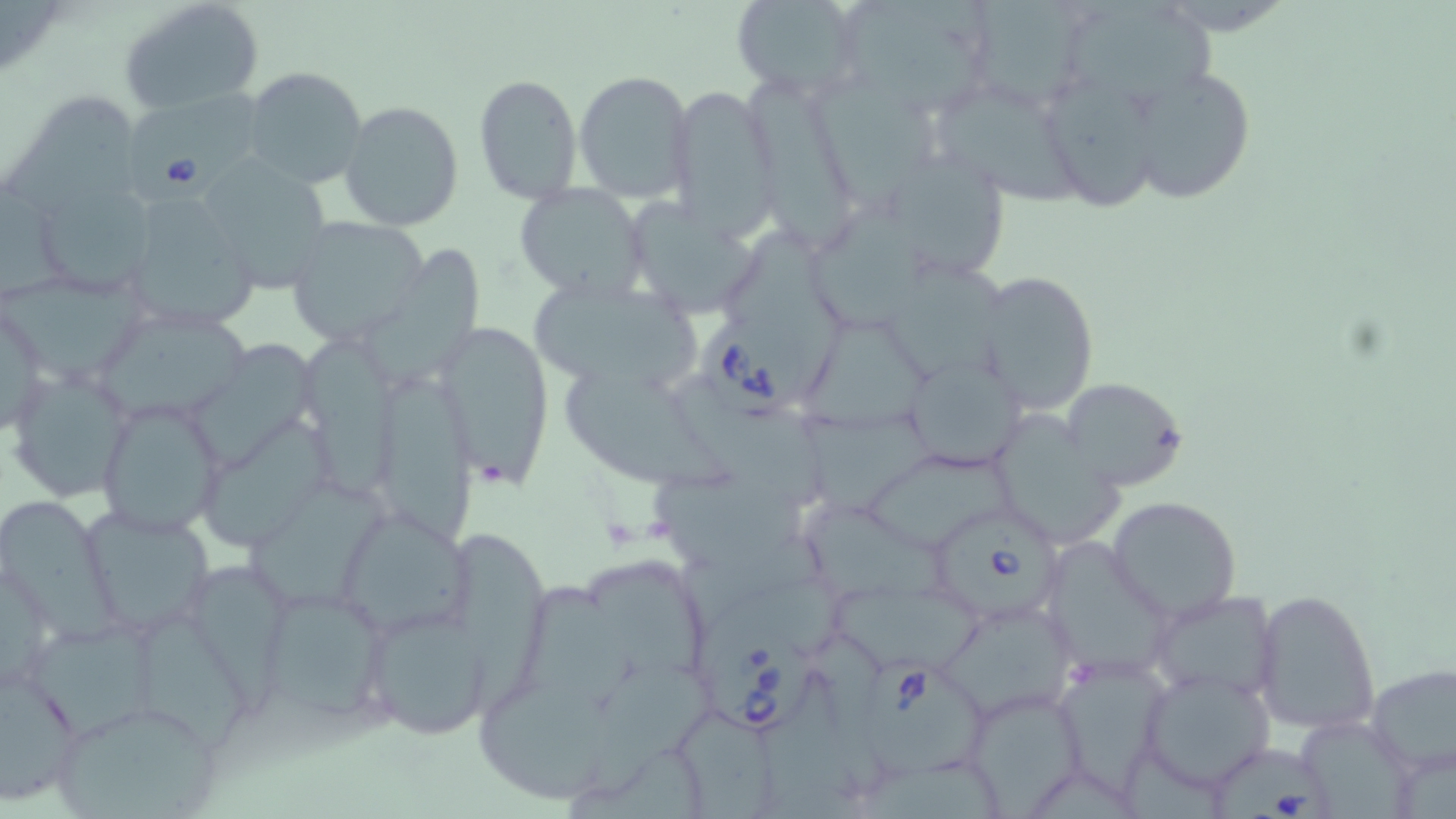

Approximate bounding boxes as [x1, y1, x2, y2] in pixels. Babesia divergens-infected red blood cell locations: [125, 86, 258, 206], [700, 317, 807, 423], [938, 513, 1071, 620], [705, 620, 817, 736], [865, 655, 990, 778], [1212, 745, 1332, 819]. Uninfected red blood cell locations: [120, 0, 263, 113], [731, 0, 867, 100], [832, 0, 1000, 120], [961, 0, 1096, 114], [1, 1, 62, 69], [1060, 3, 1226, 113], [242, 66, 369, 191], [1123, 67, 1254, 204], [573, 69, 694, 202], [473, 73, 583, 204], [752, 76, 854, 255], [1043, 78, 1164, 217], [812, 81, 951, 220], [667, 85, 781, 236], [929, 85, 1083, 211], [7, 90, 138, 223], [338, 100, 464, 232], [889, 152, 1019, 279], [194, 154, 335, 293], [35, 174, 158, 300], [0, 183, 77, 313], [514, 183, 650, 301], [118, 194, 264, 337], [619, 194, 767, 317], [812, 201, 938, 332], [287, 219, 428, 346], [724, 220, 846, 398], [360, 248, 481, 397], [889, 259, 1021, 388], [974, 269, 1100, 416], [0, 273, 149, 382], [527, 281, 708, 394], [1, 298, 49, 439], [102, 318, 254, 423], [437, 320, 553, 490], [809, 320, 945, 432], [305, 339, 403, 501], [194, 341, 317, 474], [901, 353, 1028, 473], [7, 365, 134, 500], [370, 368, 473, 555], [563, 376, 734, 494], [682, 377, 827, 513], [1059, 377, 1187, 492], [96, 397, 226, 534], [990, 405, 1133, 550], [801, 415, 942, 523], [200, 418, 333, 550], [867, 451, 1018, 551], [641, 463, 810, 577], [245, 482, 389, 609], [0, 492, 130, 647], [1107, 495, 1242, 621], [805, 506, 947, 600], [88, 509, 219, 640], [349, 520, 476, 640], [686, 525, 837, 626], [453, 529, 547, 719], [1050, 538, 1166, 686], [592, 562, 705, 683], [193, 565, 309, 719], [506, 574, 638, 721], [708, 579, 854, 656], [823, 582, 986, 678], [257, 583, 395, 731], [1253, 588, 1381, 736], [1145, 589, 1281, 702], [945, 599, 1078, 721], [362, 606, 489, 740], [146, 614, 248, 752], [27, 616, 162, 740], [1049, 655, 1174, 795], [588, 661, 716, 798], [767, 666, 851, 819], [1138, 666, 1277, 791], [1365, 666, 1455, 774], [0, 670, 82, 805], [963, 686, 1087, 813], [480, 694, 628, 803], [47, 698, 223, 819], [680, 706, 787, 819], [571, 741, 704, 819], [861, 759, 1015, 819]. Slide-level diagnosis: Babesia divergens. One field of a larger specimen. Image is 1456×819 pixels. 1000x magnification. Optical microscopy. Thin blood smear. May-Grünwald-Giemsa-stained preparation.